Assess the morphology of the red blood cells.
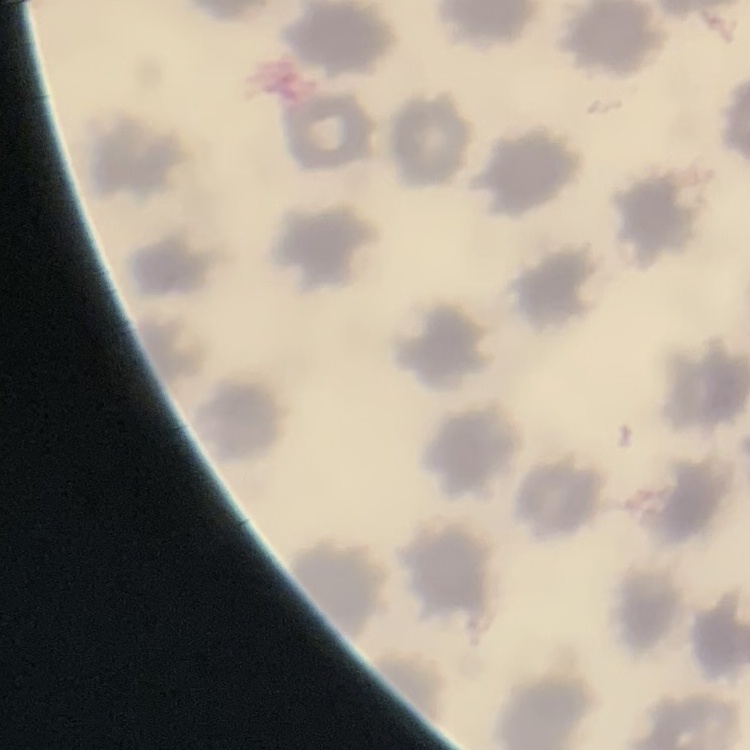

No rouleaux formation.

{
  "stain": "Field's or Giemsa",
  "preparation": "thin blood smear",
  "image_type": "one tile cut from a larger photomicrograph"
}